Comment on the morphology of the erythrocytes.
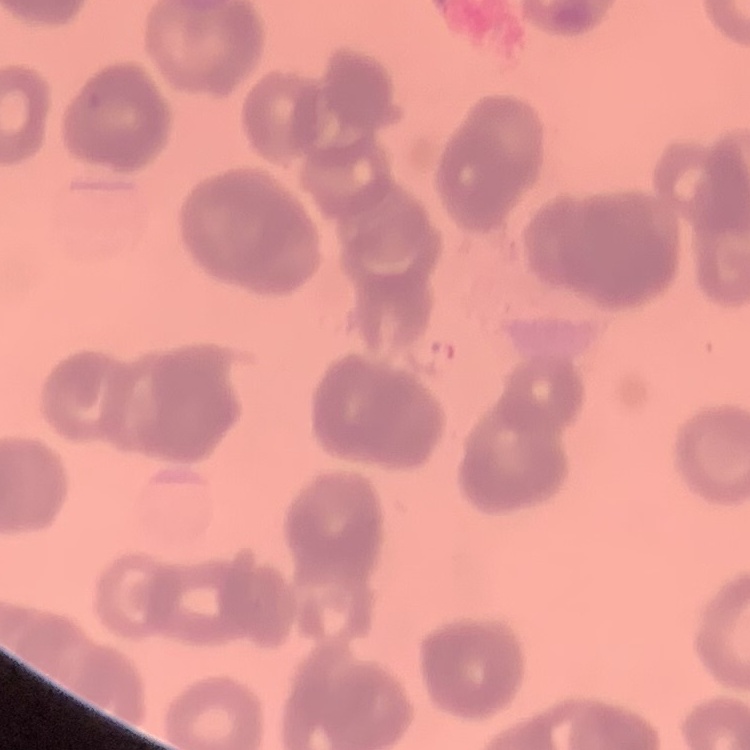
They show rouleaux formation.

preparation = thin peripheral smear
stain = Field's or Giemsa
image type = one tile cut from a larger photomicrograph